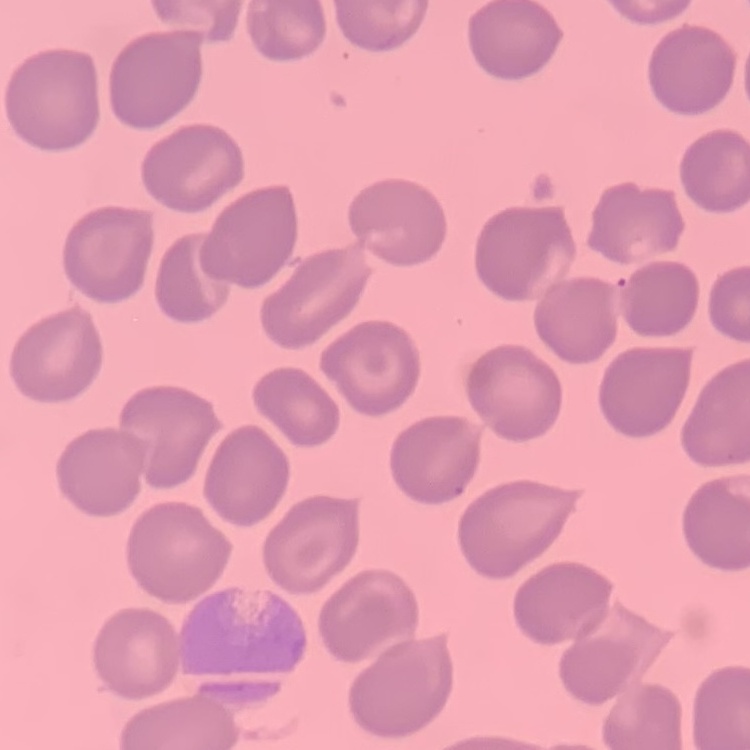

The red blood cells exhibit no rouleaux formation. One tile cut from a larger photomicrograph. Thin peripheral smear. Stained with either Field's or Giemsa.